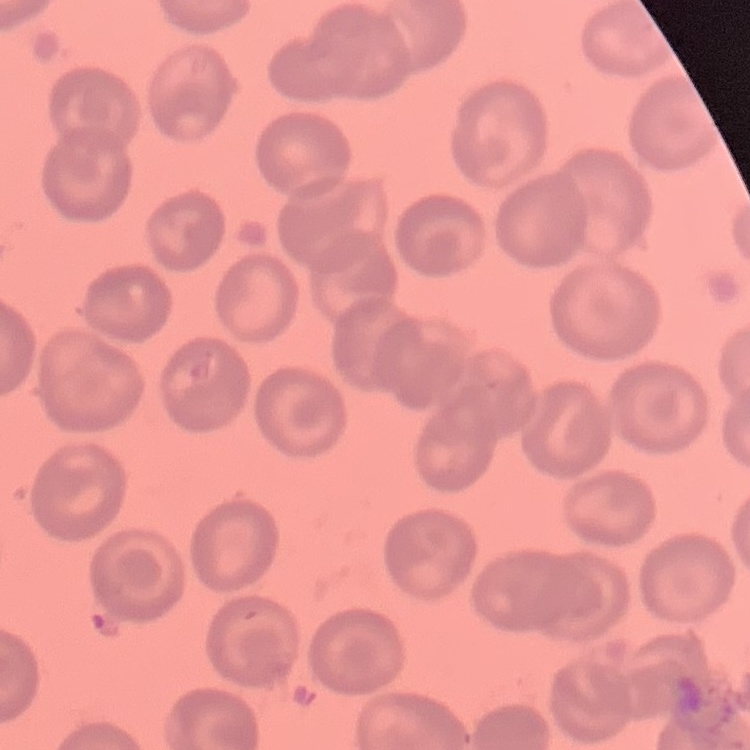 The erythrocytes exhibit no rouleaux formation. Thin blood smear. One tile cut from a larger photomicrograph. Stained with either Field's or Giemsa.